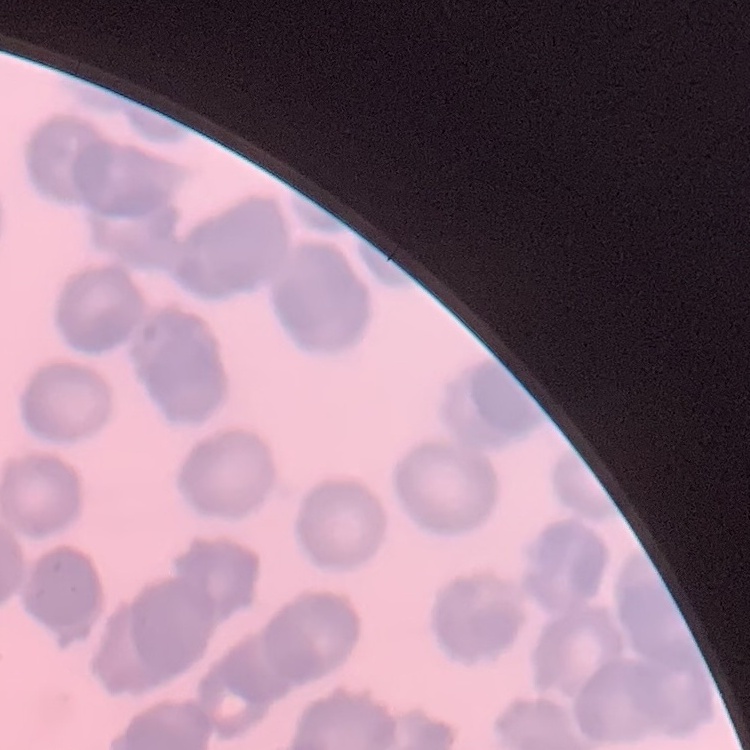

red blood cell morphology = rouleaux formation
stain = Field's or Giemsa
preparation = thin peripheral smear
image type = one tile cut from a larger photomicrograph